Locate every malaria parasite by life-cycle stage, and every leukocyte.
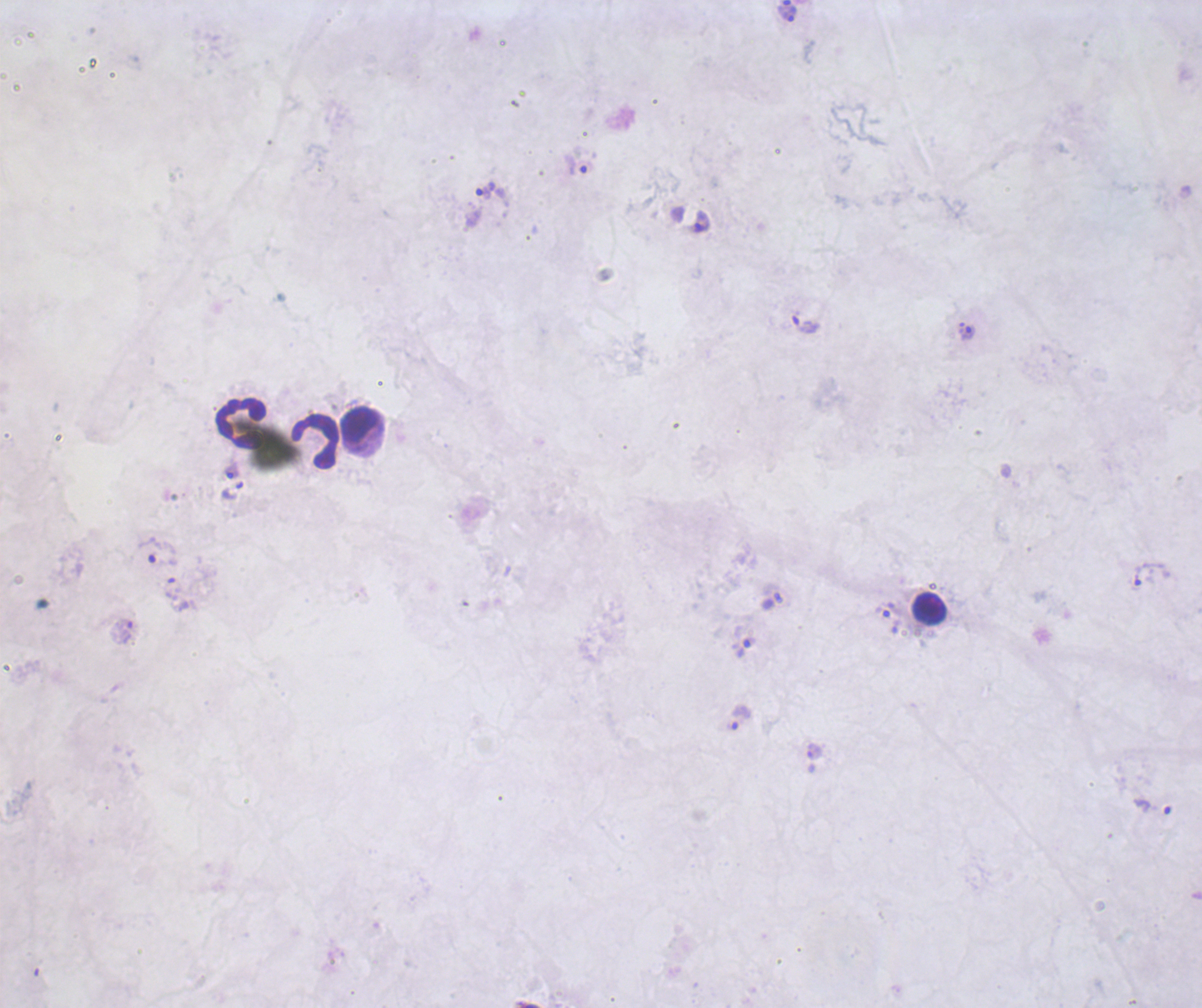

Approximate centers as {x, y} in pixels.
Trophozoites: {789, 14}, {576, 165}, {485, 190}, {702, 222}, {806, 325}, {970, 332}, {232, 471}, {232, 490}, {159, 551}, {1152, 574}, {126, 632}, {743, 648}, {740, 717}.
No schizont or gametocyte forms observed.
Leukocytes: {240, 422}, {358, 423}, {315, 441}, {928, 609}.

Summary:
  - Context: previously used in a real diagnosis
  - Background quality: good
  - Image size: 1202×1008 pixels
  - Coloration quality: bad
  - Stain: Romanowsky
  - Field of view: one from this slide
  - Magnification: 100x
  - Preparation: thick smear of blood